Locate every blood parasite and identify its species.
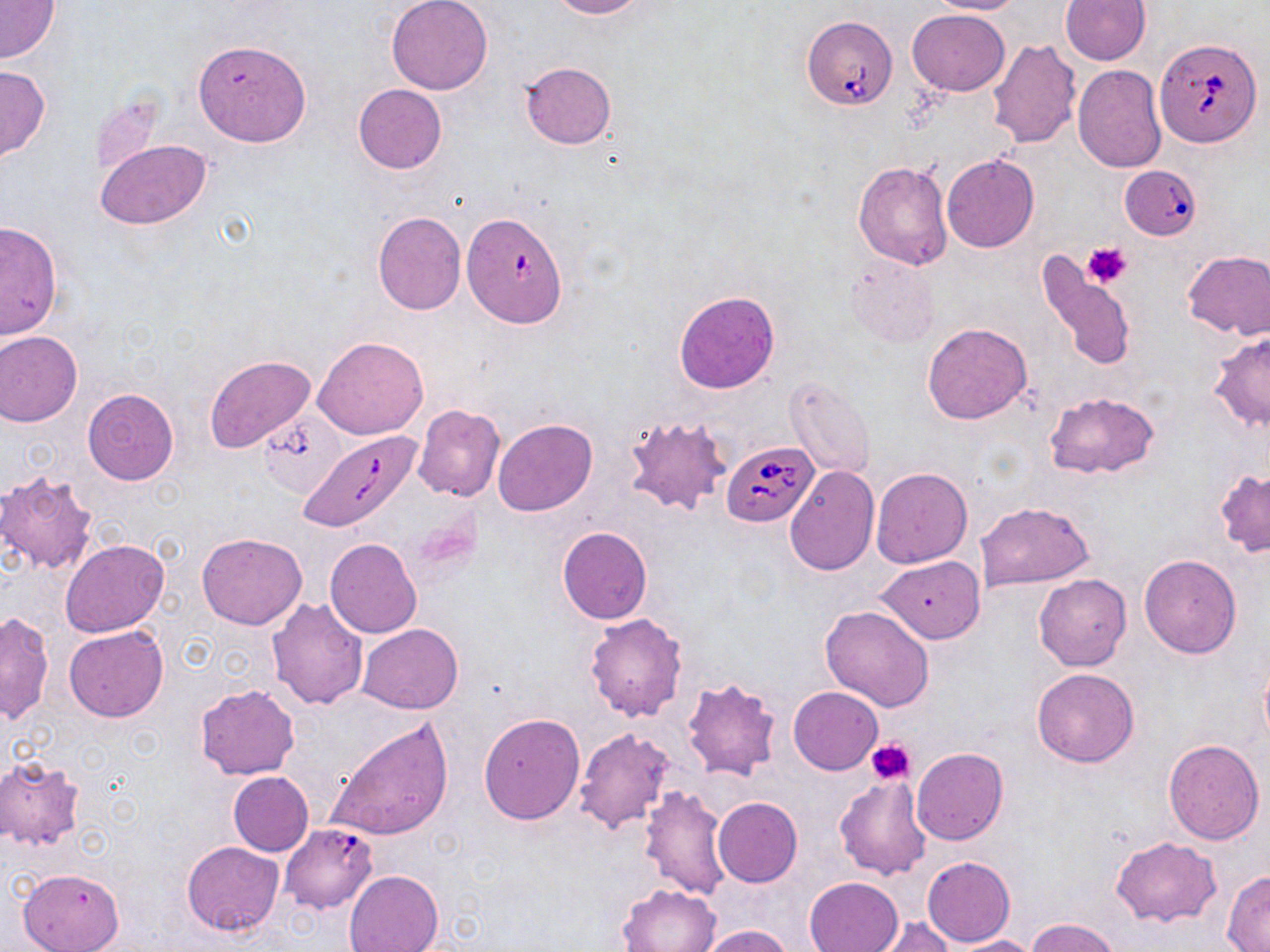

Approximate bounding boxes as (x1, y1, x2, y2) in pixels.
Babesia divergens-infected red blood cells: (802, 16, 900, 110), (1153, 35, 1265, 148), (1121, 166, 1196, 243), (454, 215, 573, 340), (302, 431, 422, 533), (723, 441, 818, 528).
No Plasmodium falciparum, Plasmodium ovale, Plasmodium malariae, Plasmodium vivax, or Trypanosoma brucei observed.

Platelet locations: (1083, 240, 1133, 289), (867, 736, 916, 785). Uninfected red blood cell locations: (386, 0, 492, 95), (547, 0, 646, 18), (928, 0, 1025, 15), (1060, 0, 1150, 66), (0, 1, 61, 63), (908, 9, 1010, 96), (193, 38, 310, 147), (987, 39, 1081, 148), (520, 61, 617, 150), (0, 63, 50, 163), (1073, 65, 1167, 173), (353, 84, 446, 175), (88, 90, 166, 181), (95, 139, 211, 231), (941, 154, 1039, 252), (852, 161, 953, 270), (372, 212, 466, 314), (0, 221, 62, 339), (1182, 249, 1270, 341), (1034, 254, 1140, 374), (847, 256, 940, 346), (673, 291, 779, 394), (921, 322, 1033, 425), (0, 330, 81, 426), (1206, 333, 1270, 434), (313, 336, 429, 439), (204, 354, 315, 452), (785, 377, 875, 478), (82, 387, 179, 485), (1042, 391, 1160, 480), (411, 404, 505, 502), (623, 413, 733, 518), (493, 418, 598, 515), (784, 466, 879, 573), (871, 468, 972, 569), (1214, 468, 1270, 559), (0, 469, 100, 576), (975, 501, 1094, 591), (557, 526, 652, 624), (196, 533, 307, 630), (59, 538, 169, 637), (325, 538, 422, 639), (1140, 554, 1241, 658), (878, 556, 984, 644), (1034, 574, 1131, 670), (267, 597, 369, 711), (821, 604, 935, 711), (1, 611, 55, 725), (584, 613, 687, 721), (356, 624, 463, 714), (63, 625, 169, 722), (1259, 654, 1270, 749), (1032, 668, 1139, 767), (682, 677, 781, 781), (196, 684, 300, 779), (789, 687, 882, 774), (478, 714, 584, 825), (326, 717, 454, 842), (574, 728, 677, 834), (1163, 738, 1265, 843), (912, 747, 1008, 845), (0, 757, 87, 850), (227, 772, 314, 856), (834, 776, 933, 881), (638, 784, 731, 901), (713, 796, 802, 887), (281, 823, 377, 913), (1110, 836, 1222, 927), (182, 841, 284, 937), (923, 856, 1015, 947), (17, 867, 125, 952), (344, 870, 443, 952), (1223, 871, 1270, 950), (804, 876, 902, 952), (618, 882, 722, 952), (868, 916, 957, 952), (1026, 917, 1123, 952), (695, 925, 792, 952), (948, 935, 1042, 952). Slide-level diagnosis: Babesia divergens. Image is 1270×952 pixels. Optical microscopy. May-Grünwald-Giemsa stain. Single field of view. 1000x magnification. Thin blood film.